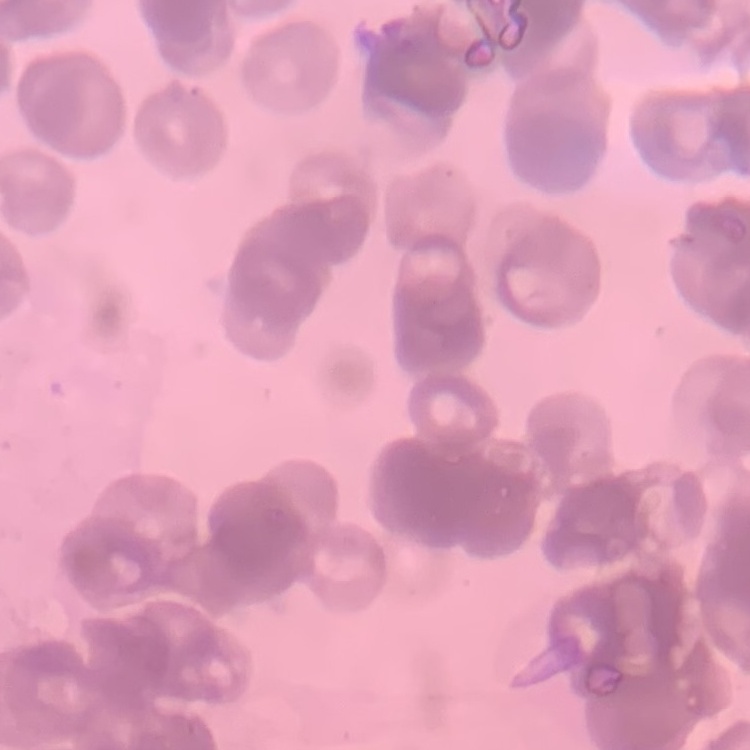
Summary:
  - Red blood cell morphology: rouleaux formation
  - Stain: Field's or Giemsa
  - Image type: one tile cut from a larger photomicrograph
  - Preparation: thin blood smear